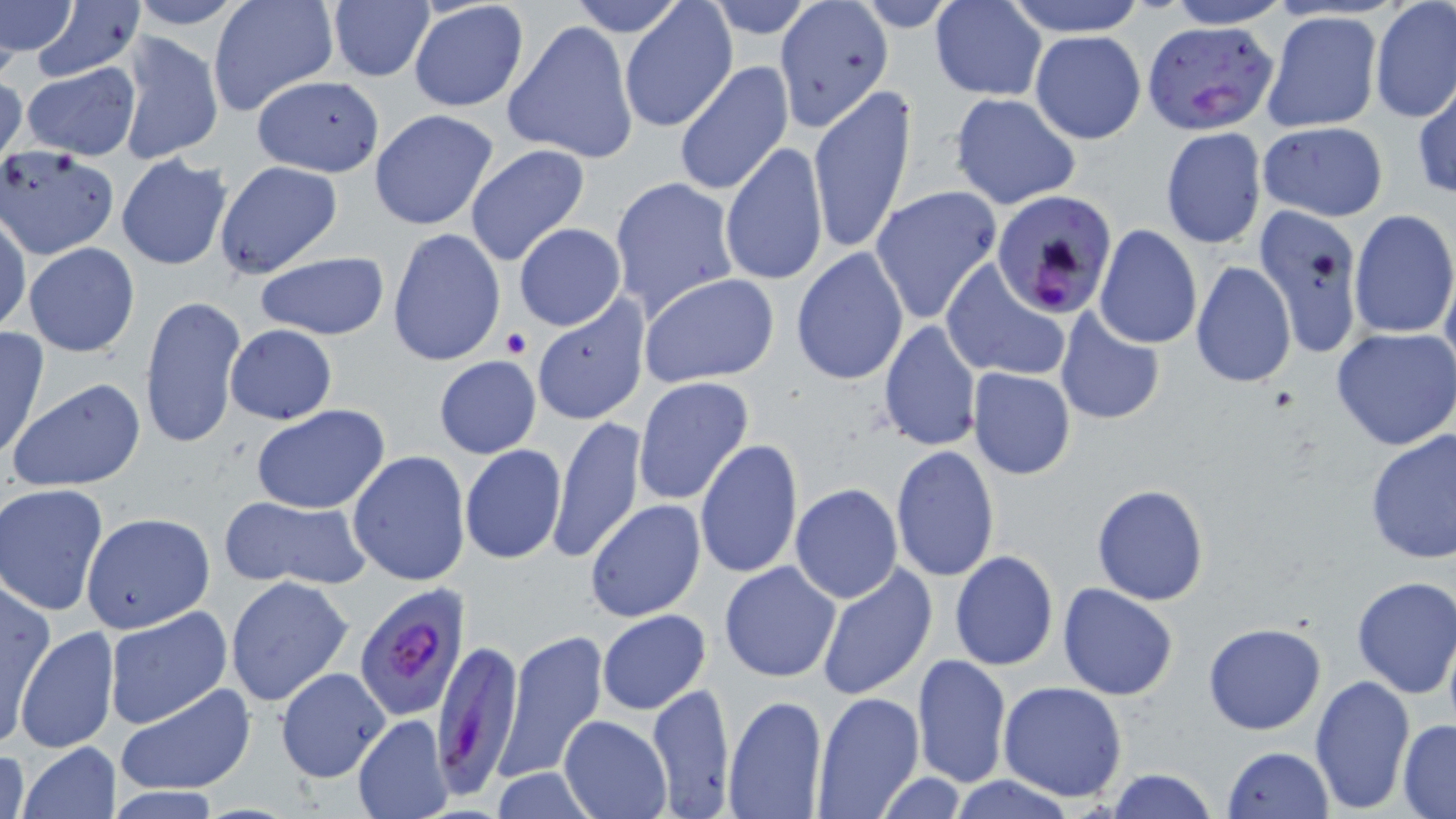

Summary:
  - Coordinate format: approximate bounding boxes as (x1,y1)-(x2,y2) corner pairs in pixels
  - Plasmodium falciparum-infected red blood cell locations: (1142,19)-(1279,134), (990,189)-(1120,321), (352,585)-(472,721), (431,639)-(525,796)
  - Uninfected red blood cell locations: (0,0)-(80,56), (124,0)-(255,31), (209,0)-(338,117), (567,0)-(689,37), (705,0)-(818,39), (1003,0)-(1148,37), (1164,0)-(1295,28), (773,1)-(894,132), (853,1)-(967,31), (930,1)-(1048,100), (1369,1)-(1456,122), (327,2)-(435,82), (26,3)-(145,82), (408,3)-(530,113), (620,3)-(735,131), (1262,11)-(1383,132), (504,22)-(638,164), (1029,29)-(1147,143), (115,30)-(223,167), (672,60)-(794,197), (21,62)-(141,161), (0,70)-(26,169), (250,74)-(385,176), (1413,79)-(1455,200), (808,84)-(917,255), (949,92)-(1082,211), (369,109)-(498,231), (1258,122)-(1389,222), (1160,127)-(1267,249), (719,141)-(828,290), (465,144)-(590,266), (115,154)-(233,270), (213,160)-(343,278), (609,176)-(739,321), (869,184)-(1002,324), (1253,205)-(1365,358), (1348,210)-(1456,339), (0,214)-(29,337), (513,223)-(627,332), (1095,225)-(1203,349), (387,227)-(505,367), (23,242)-(139,356), (789,248)-(909,384), (253,251)-(390,340), (1191,260)-(1296,389), (1440,260)-(1456,386), (942,261)-(1069,383), (640,274)-(780,387), (139,294)-(247,450), (532,297)-(650,426), (1054,305)-(1169,425), (878,319)-(981,453), (225,324)-(337,424), (0,327)-(49,462), (1332,327)-(1456,449), (433,356)-(541,458), (968,368)-(1075,479), (632,376)-(755,506), (10,377)-(146,492), (251,403)-(390,514), (549,416)-(646,565), (1364,429)-(1455,564), (695,439)-(804,580), (890,444)-(1000,581), (459,445)-(567,564), (348,450)-(471,588), (790,483)-(904,603), (1,484)-(112,617), (1091,484)-(1210,605), (221,496)-(371,591), (586,500)-(706,621), (80,512)-(215,633), (949,550)-(1058,671), (718,561)-(841,682), (814,564)-(938,700), (225,575)-(353,707), (1350,575)-(1456,698), (0,580)-(55,744), (1058,584)-(1178,700), (104,608)-(232,728), (598,609)-(711,715), (1203,623)-(1327,734), (14,625)-(121,753), (496,629)-(608,782), (912,654)-(1012,788), (275,667)-(390,782), (1308,673)-(1414,814), (648,681)-(735,816), (998,681)-(1128,803), (115,682)-(258,797), (812,691)-(923,818), (722,694)-(825,818), (354,714)-(454,818), (560,715)-(670,819), (1398,721)-(1456,817), (17,740)-(122,818), (1,746)-(30,819), (1220,746)-(1334,819), (1106,767)-(1218,819), (488,768)-(604,818), (873,774)-(971,816), (945,776)-(1076,818)
  - Platelet locations: (500,328)-(531,357)
  - Slide-level diagnosis: Plasmodium falciparum
  - Modality: light microscopy
  - Image size: 1456×819 pixels
  - Magnification: 1000x
  - Preparation: thin blood film
  - Stain: May-Grünwald-Giemsa
  - Field of view: single